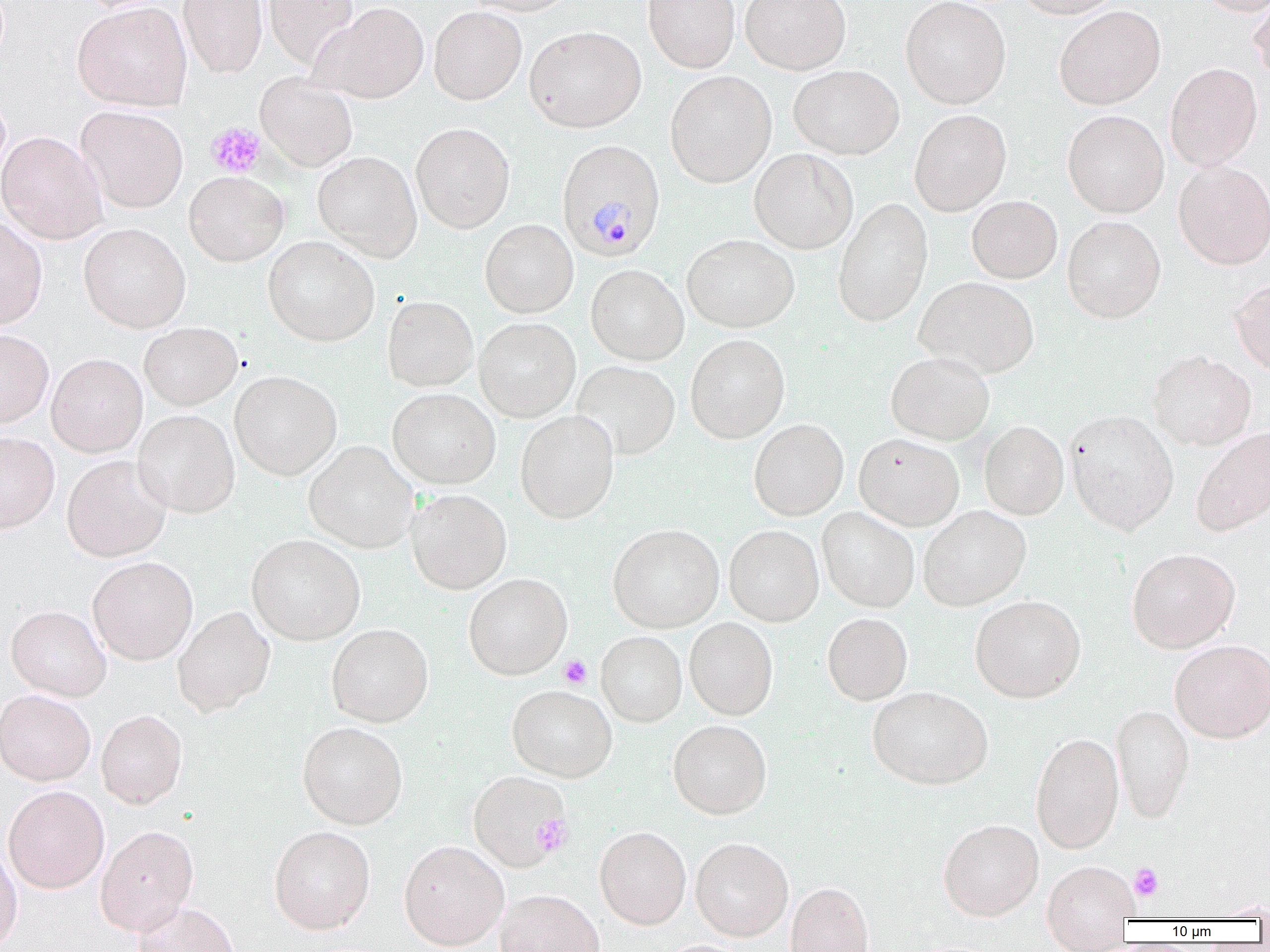

Approximate bounding boxes as (x1,y1)-(x2,y2) corner pairs in pixels. Platelet locations: (206,121)-(266,178), (559,655)-(591,688), (533,814)-(573,855), (1129,863)-(1164,901). Plasmodium malariae-infected red blood cell locations: (556,139)-(666,262). Uninfected red blood cell locations: (178,0)-(267,78), (263,0)-(359,69), (460,0)-(581,16), (643,0)-(740,73), (740,0)-(851,74), (900,0)-(1011,109), (1015,0)-(1122,19), (1196,0)-(1270,16), (1249,0)-(1270,84), (72,2)-(191,110), (311,2)-(429,104), (429,6)-(527,105), (1054,6)-(1165,110), (525,25)-(646,132), (1165,63)-(1263,170), (788,64)-(904,159), (665,71)-(776,187), (255,73)-(358,172), (75,105)-(188,213), (909,109)-(1012,216), (1063,110)-(1169,217), (410,122)-(515,233), (0,131)-(108,244), (749,148)-(858,254), (313,151)-(422,262), (1172,160)-(1270,270), (183,171)-(288,266), (967,195)-(1063,283), (833,198)-(933,327), (1062,215)-(1166,323), (0,216)-(47,331), (480,219)-(578,318), (78,223)-(191,333), (682,234)-(799,333), (263,235)-(380,346), (586,264)-(688,365), (915,276)-(1039,379), (1230,279)-(1270,377), (382,295)-(479,391), (474,318)-(581,422), (139,322)-(243,410), (0,329)-(53,429), (685,334)-(790,443), (1147,350)-(1257,451), (886,351)-(995,445), (46,353)-(148,457), (572,361)-(680,460), (230,370)-(342,480), (387,388)-(501,489), (132,410)-(240,518), (515,410)-(619,523), (1065,410)-(1179,535), (749,419)-(849,520), (979,420)-(1069,520), (1190,427)-(1270,537), (0,431)-(60,533), (854,433)-(964,531), (303,441)-(419,553), (61,455)-(172,562), (407,489)-(512,594), (918,505)-(1031,610), (817,507)-(920,612), (607,524)-(724,633), (724,525)-(824,626), (246,534)-(366,645), (1126,548)-(1240,653), (87,556)-(198,665), (463,573)-(572,679), (970,594)-(1086,702), (6,605)-(111,701), (172,606)-(276,716), (822,613)-(913,705), (684,617)-(778,720), (326,623)-(434,727), (596,631)-(687,726), (1169,639)-(1270,743), (507,685)-(617,782), (867,686)-(993,789), (0,689)-(96,786), (1111,703)-(1194,824), (95,709)-(187,809), (668,720)-(772,818), (297,721)-(408,830), (1031,732)-(1123,853), (467,770)-(572,871), (3,785)-(110,893), (938,819)-(1044,921), (95,824)-(199,935), (269,825)-(376,934), (595,826)-(691,929), (690,837)-(793,941), (399,839)-(509,950), (0,841)-(23,952), (1042,859)-(1138,944), (786,881)-(873,952), (494,889)-(605,952), (1207,898)-(1270,920), (132,901)-(240,952). Slide-level diagnosis: Plasmodium malariae. 1000x magnification. Thin blood film. Image is 1270×952 pixels. Optical microscopy. One field of a larger specimen.